Assess this cell for malaria.
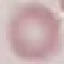
Uninfected.

Automatically extracted cell patch, resized to 64 × 64 pixels. Photographed with a smartphone camera at the microscope eyepiece. Giemsa-stained preparation. Thin blood smear.